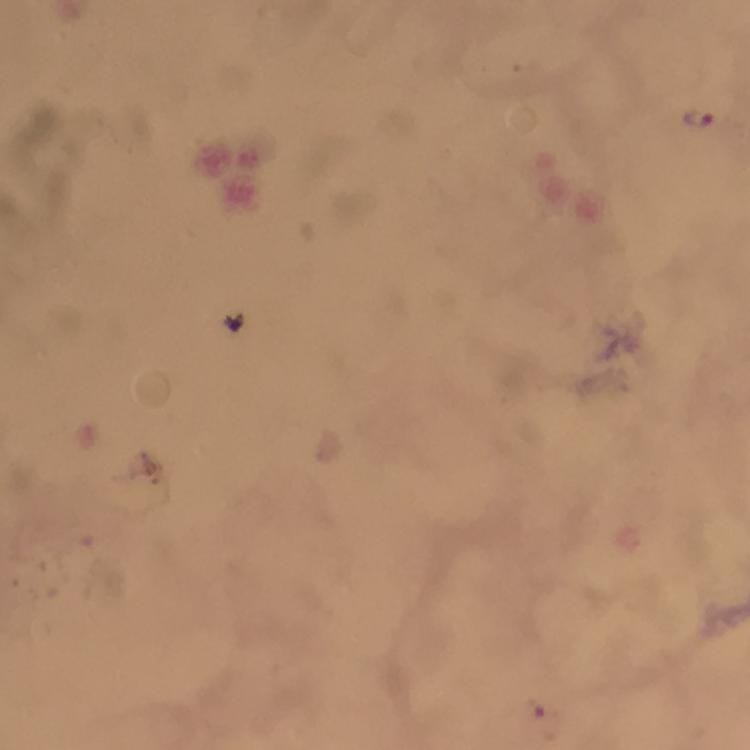 Approximate centers as [x, y] in pixels. Malaria parasite locations: [701, 118]. Image is 750×750 pixels. Giemsa-stained preparation. Photographed through the microscope with a smartphone camera. At 100x magnification. Thick blood film. From a malaria diagnostic workup. A crop from one field of view. Immersion oil was used.